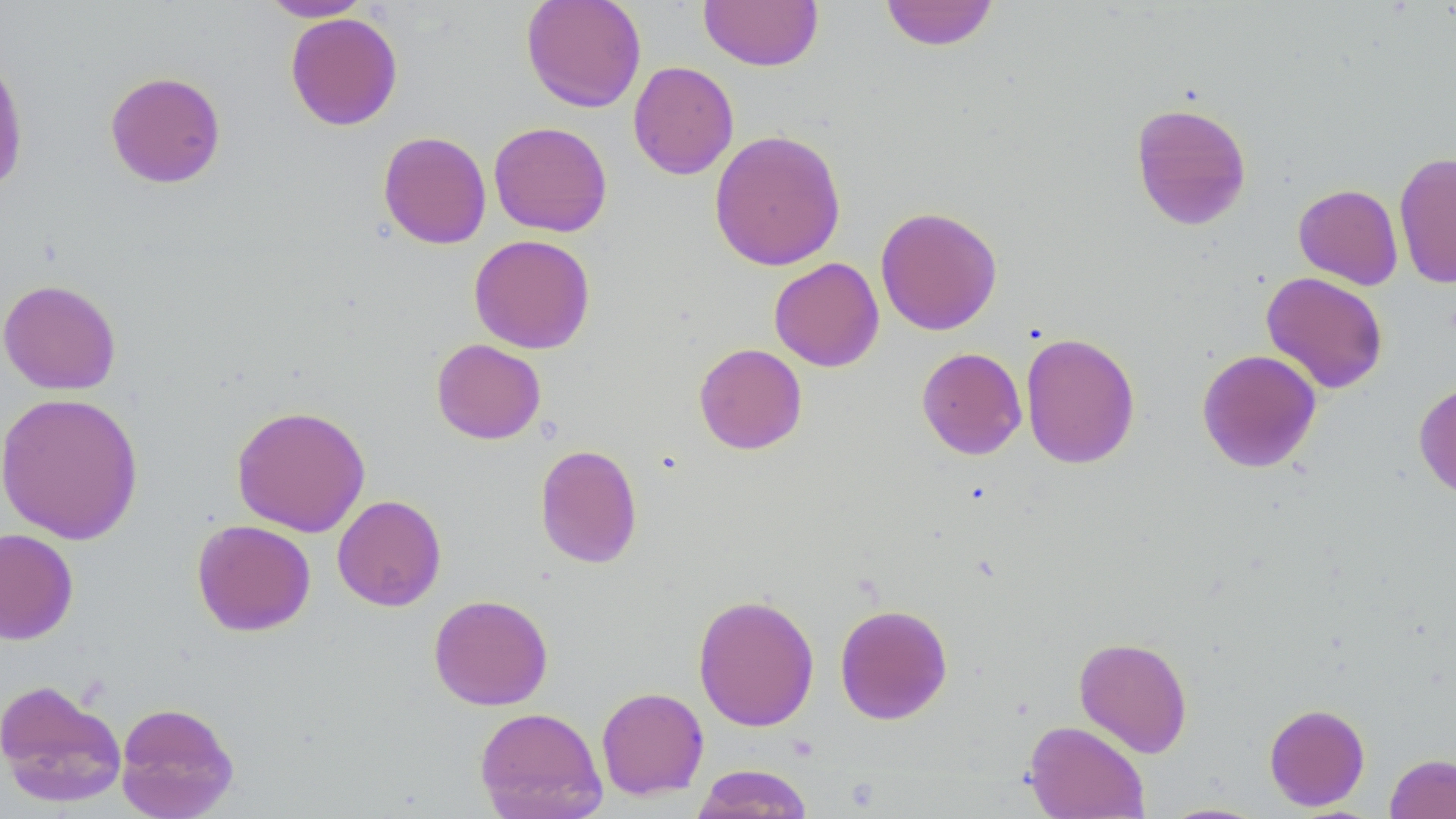 Approximate bounding boxes as (x1,y1)-(x2,y2) corner pairs in pixels. Uninfected red blood cell locations: (259,0)-(372,22), (521,0)-(646,113), (698,0)-(824,71), (879,0)-(1000,51), (285,12)-(403,131), (0,49)-(30,195), (627,61)-(739,180), (104,70)-(227,188), (1130,101)-(1252,231), (488,121)-(612,237), (709,129)-(846,271), (378,131)-(492,250), (1394,151)-(1456,288), (1293,184)-(1403,290), (875,206)-(1003,336), (469,234)-(596,354), (768,257)-(884,372), (1261,271)-(1389,394), (0,279)-(122,395), (1020,332)-(1141,469), (431,339)-(545,445), (694,343)-(807,454), (917,347)-(1027,460), (1197,349)-(1321,473), (1414,379)-(1456,499), (0,392)-(144,545), (231,405)-(370,537), (534,443)-(643,568), (332,495)-(446,611), (192,519)-(315,636), (0,528)-(79,644), (692,592)-(819,732), (428,594)-(553,711), (834,604)-(953,724), (1074,636)-(1193,757), (0,678)-(127,807), (596,686)-(709,800), (115,702)-(239,818), (1264,703)-(1370,811), (474,706)-(607,819), (1024,720)-(1149,818), (1385,752)-(1456,819), (690,764)-(815,818), (1158,801)-(1273,818). Slide-level diagnosis: negative for blood parasites. Optical microscopy. Image is 1456×819 pixels. Thin blood film. One field of a larger specimen. May-Grünwald-Giemsa-stained preparation. 1000x magnification.